Name the cell type shown.
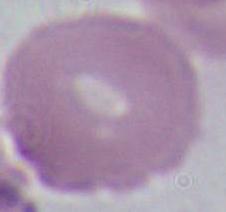
An erythrocyte.

magnification = 1000x
modality = photomicrograph